State which parasite is depicted.
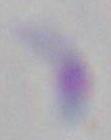

Toxoplasma gondii.

1000x magnification. Photomicrograph.